Assess this cell for malaria.
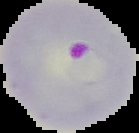

Parasitized.

Image is 139×133 pixels. The area outside the segmented cell region is set to black. From a thin blood smear.